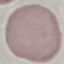

result: no malaria parasites seen
capture: smartphone camera at the microscope eyepiece
preparation: thin smear
image_type: automatically extracted cell patch, resized to 64 × 64 pixels
stain: Giemsa